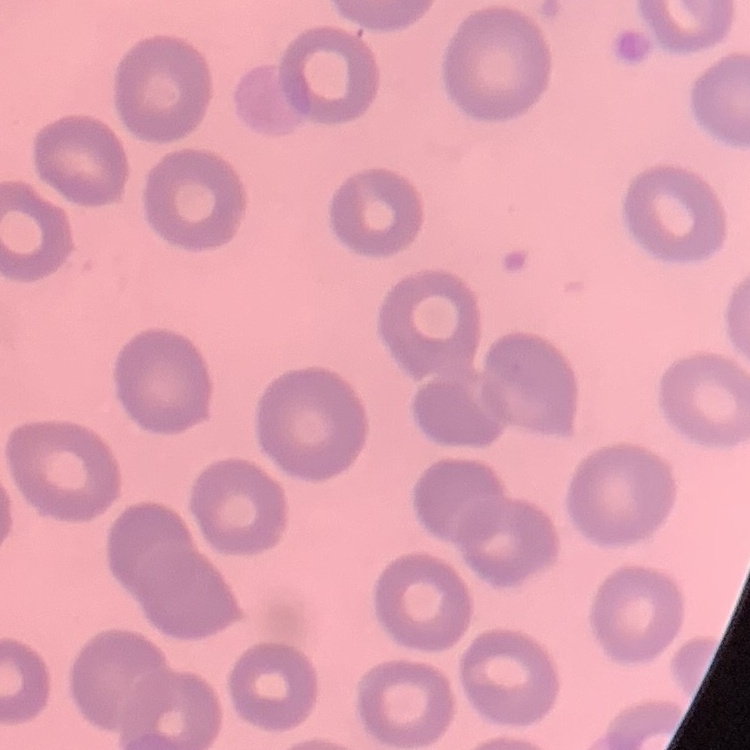

The red blood cells exhibit no rouleaux formation. Thin blood film. Stained with either Field's or Giemsa. Square crop of a larger photomicrograph.